Outline each blood parasite and name the species.
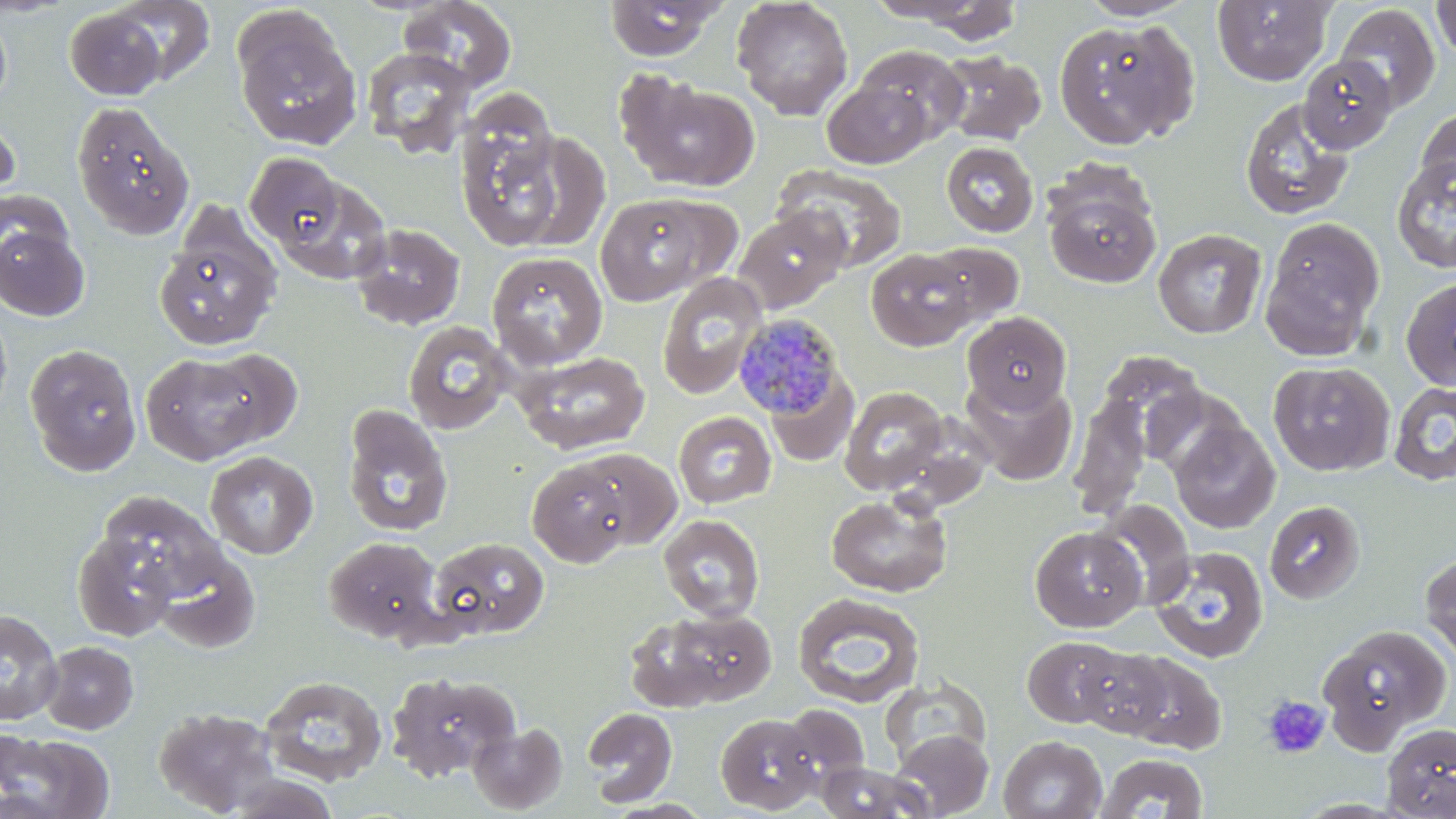
Approximate bounding boxes as [x1, y1, x2, y2] in pixels.
Plasmodium malariae-infected red blood cells: [734, 313, 848, 422].
No Plasmodium falciparum, Plasmodium ovale, Plasmodium vivax, Babesia divergens, or Trypanosoma brucei observed.

Summary:
  - Uninfected red blood cell locations: [398, 0, 517, 91], [602, 0, 726, 61], [732, 0, 854, 120], [1076, 0, 1198, 21], [1212, 0, 1336, 86], [103, 1, 218, 88], [890, 1, 1025, 42], [1431, 1, 1456, 62], [1335, 4, 1440, 114], [0, 7, 12, 109], [63, 7, 170, 100], [231, 11, 362, 150], [1053, 18, 1199, 149], [855, 45, 969, 146], [361, 47, 476, 158], [937, 50, 1046, 145], [1299, 55, 1398, 153], [617, 74, 760, 193], [823, 79, 934, 169], [1240, 98, 1355, 221], [71, 101, 193, 240], [456, 107, 572, 253], [1415, 107, 1456, 201], [0, 109, 21, 213], [941, 141, 1039, 237], [244, 153, 347, 251], [1392, 155, 1456, 274], [774, 166, 908, 272], [275, 174, 392, 286], [1043, 183, 1162, 288], [0, 189, 74, 285], [594, 194, 715, 306], [733, 207, 849, 314], [0, 216, 91, 321], [1261, 216, 1385, 359], [154, 221, 282, 352], [350, 223, 466, 330], [1152, 228, 1266, 339], [923, 242, 1024, 327], [865, 248, 978, 351], [487, 251, 608, 369], [657, 272, 767, 399], [1401, 276, 1456, 392], [0, 306, 12, 423], [962, 312, 1071, 414], [403, 321, 514, 434], [24, 344, 143, 476], [202, 348, 303, 446], [515, 351, 650, 455], [142, 353, 265, 465], [1268, 361, 1395, 477], [765, 371, 858, 466], [960, 374, 1077, 486], [1388, 382, 1456, 486], [1142, 385, 1248, 480], [840, 386, 949, 495], [1069, 394, 1151, 519], [342, 404, 454, 537], [673, 411, 776, 508], [1170, 418, 1280, 534], [572, 448, 682, 551], [205, 451, 318, 559], [527, 458, 636, 567], [97, 491, 227, 605], [825, 493, 952, 597], [1093, 499, 1195, 609], [1264, 500, 1365, 603], [658, 514, 765, 622], [1029, 526, 1146, 631], [73, 530, 180, 641], [323, 536, 443, 643], [426, 536, 550, 640], [152, 546, 262, 654], [1149, 546, 1269, 663], [1421, 552, 1456, 664], [792, 593, 924, 708], [0, 608, 63, 725], [643, 608, 778, 708], [1317, 623, 1451, 750], [1022, 636, 1130, 729], [40, 641, 138, 734], [1070, 642, 1178, 740], [1109, 650, 1227, 755], [384, 671, 519, 783], [259, 674, 387, 785], [880, 676, 991, 768], [781, 704, 870, 788], [153, 706, 282, 816], [582, 707, 677, 807], [715, 713, 822, 813], [468, 722, 567, 813], [1381, 723, 1456, 818], [2, 730, 114, 819], [892, 730, 994, 817], [998, 735, 1108, 819], [1095, 753, 1208, 819], [816, 761, 929, 819], [223, 773, 341, 818], [607, 799, 715, 818]
  - Platelet locations: [1261, 694, 1331, 759]
  - Slide-level diagnosis: Plasmodium malariae
  - Field of view: one of a larger specimen
  - Stain: May-Grünwald-Giemsa
  - Modality: light microscopy
  - Preparation: thin blood smear
  - Image size: 1456×819 pixels
  - Magnification: 1000x